Identify the parasite.
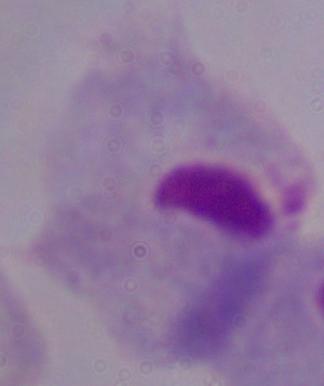
This is a trichomonad.

Photomicrograph. 1000x magnification.